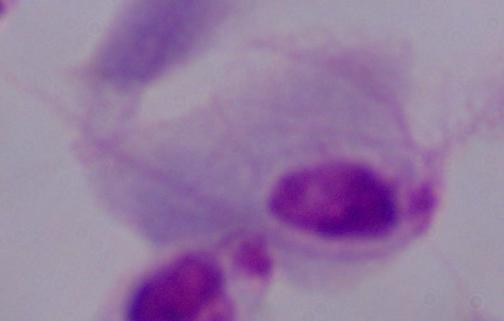
{
  "identification": "trichomonad",
  "magnification": "1000x",
  "modality": "photomicrograph"
}